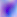

Summary:
  - Modality: photomicrograph
  - Magnification: 400x
  - Identification: Toxoplasma gondii